Assess the morphology of the red blood cells.
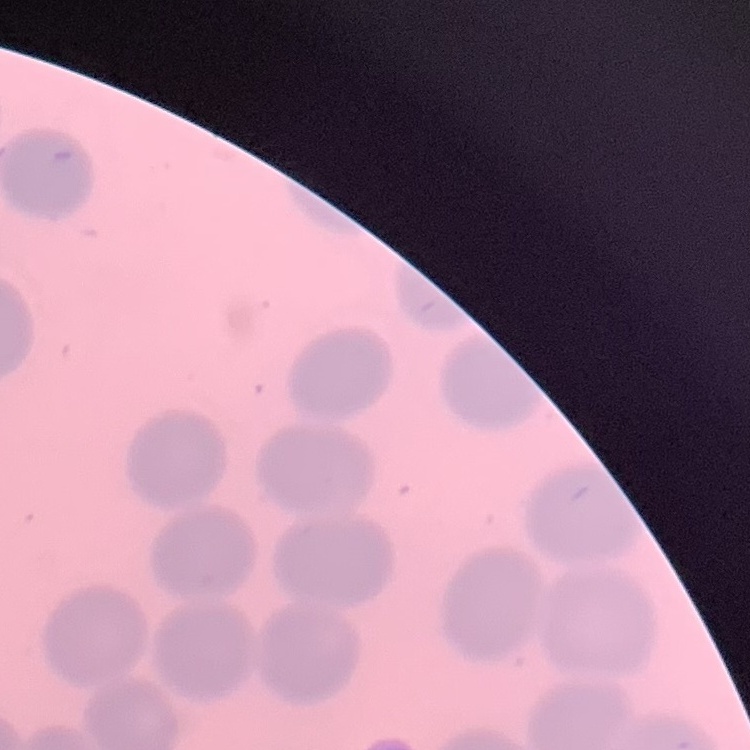

No rouleaux formation.

Field's or Giemsa stain. Thin peripheral smear. Square crop of a larger photomicrograph.